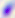
Summary:
  - Modality: photomicrograph
  - Identification: Toxoplasma gondii
  - Magnification: 400x